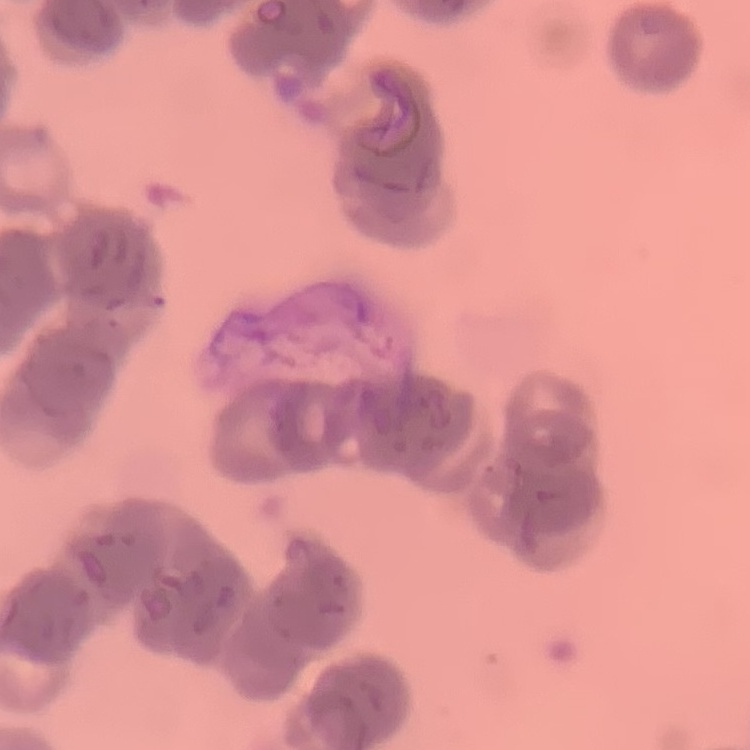

The erythrocytes exhibit rouleaux formation. Stained with either Field's or Giemsa. One tile cut from a larger photomicrograph. Thin peripheral smear.